Classify this cell by malaria status.
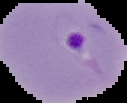

It is parasitized.

image_size: 127×103 pixels
preparation: thin blood smear
image_type: segmented cell region with the area outside set to black